Assess the morphology of the erythrocytes.
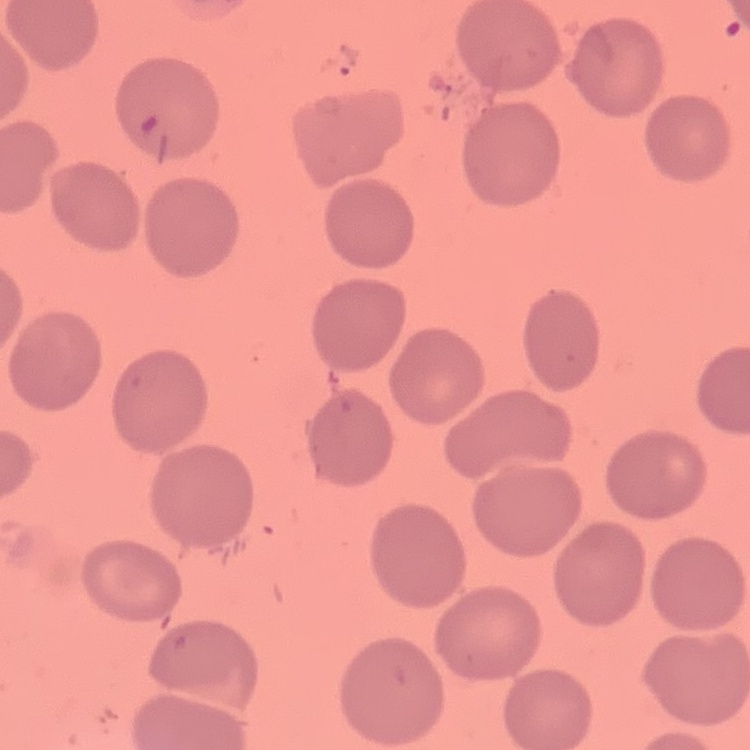
They show no rouleaux formation.

Summary:
  - Image type: one tile cut from a larger photomicrograph
  - Preparation: thin peripheral smear
  - Stain: Field's or Giemsa